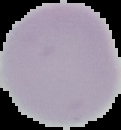
Image is 121×130 pixels. Result: no malaria parasites seen. From a thin blood smear. Cell region segmented out of the field of view; the surrounding area is masked to black.